Classify this cell by malaria status.
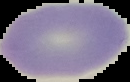
Uninfected.

Summary:
  - Preparation: thin blood smear
  - Image type: segmented cell region on a black background
  - Image size: 130×82 pixels